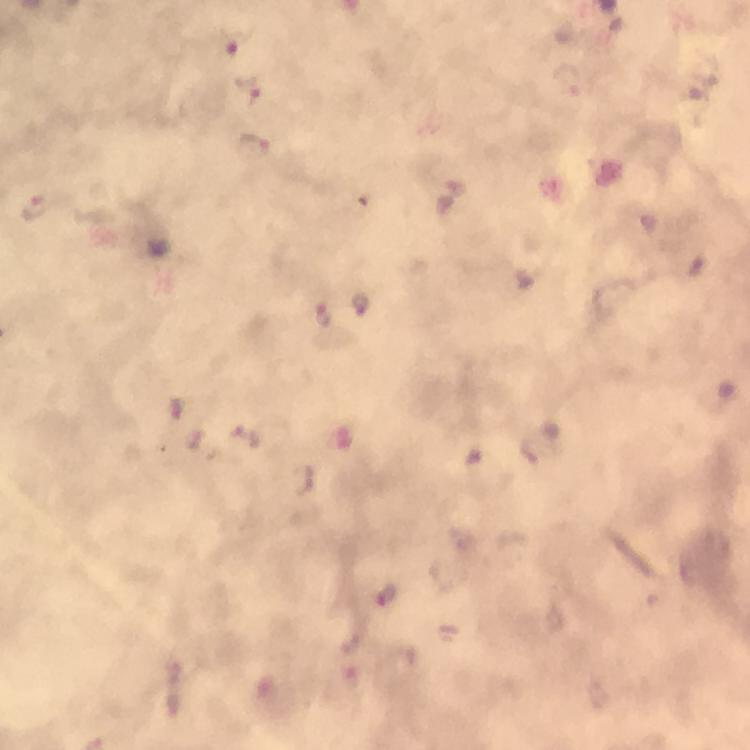

Approximate centers as (x, y) in pixels.
Summary:
  - Malaria parasite locations: (233, 43), (248, 88), (253, 147), (39, 208), (360, 304), (324, 315), (178, 408), (387, 596)
  - Context: from a diagnostic examination for malaria
  - Preparation: thick smear
  - Immersion oil: used
  - Magnification: 100x
  - Capture: smartphone mounted on the microscope
  - Stain: Giemsa
  - Cropped from: a single field of view
  - Image size: 750×750 pixels